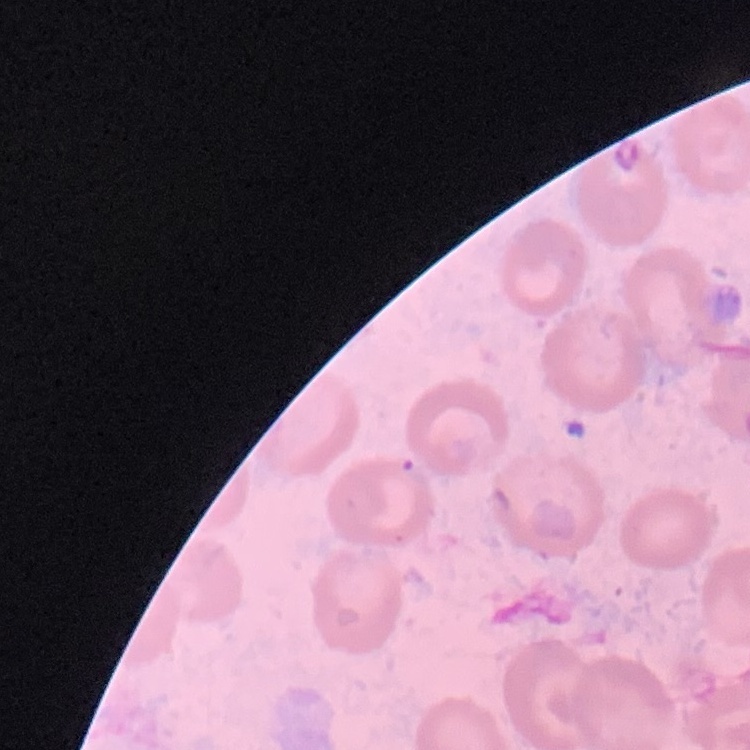
erythrocyte morphology = no rouleaux formation
image type = one tile cut from a larger photomicrograph
stain = Field's or Giemsa
preparation = thin peripheral smear